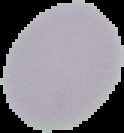
result = no Plasmodium parasites detected
preparation = thin blood smear
image size = 124×133 pixels
image type = segmented cell region with the area outside set to black